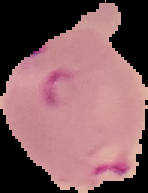

Image is 148×193 pixels. The area outside the segmented cell region is set to black. Malaria status: parasitized. From a thin blood smear.